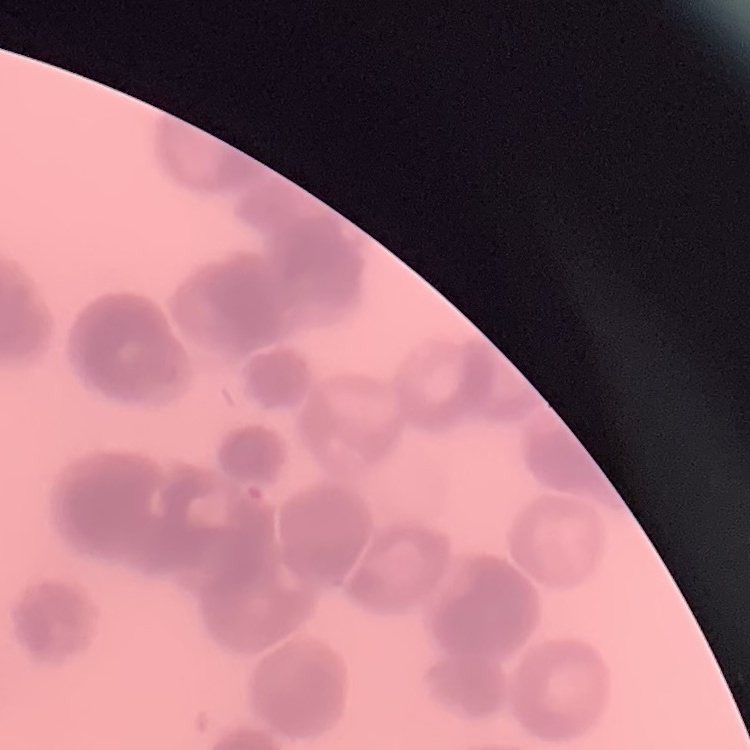

The erythrocytes exhibit rouleaux formation. One tile cut from a larger photomicrograph. Stained with either Field's or Giemsa. Thin peripheral smear.